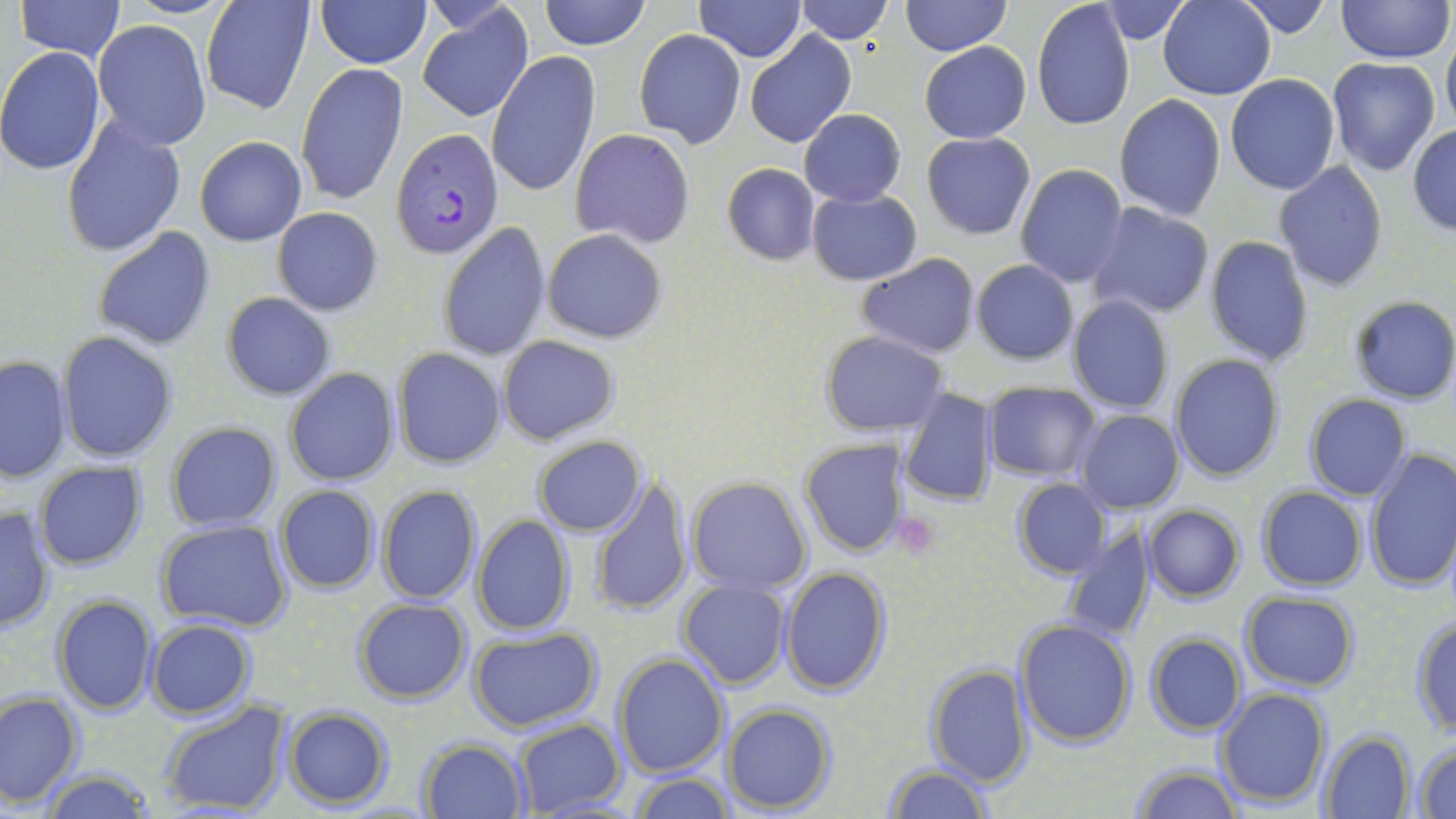 Approximate bounding boxes as named x1/y1/x2/y2 corners in pixels. Platelet locations: (x1=890, y1=513, x2=941, y2=558). Plasmodium falciparum-infected red blood cell locations: (x1=392, y1=127, x2=503, y2=259). Uninfected red blood cell locations: (x1=15, y1=0, x2=126, y2=61), (x1=117, y1=0, x2=240, y2=18), (x1=200, y1=0, x2=315, y2=115), (x1=316, y1=0, x2=430, y2=69), (x1=539, y1=0, x2=651, y2=50), (x1=695, y1=0, x2=805, y2=62), (x1=794, y1=0, x2=893, y2=44), (x1=901, y1=0, x2=1009, y2=57), (x1=1158, y1=0, x2=1275, y2=99), (x1=1233, y1=0, x2=1335, y2=39), (x1=1335, y1=0, x2=1454, y2=65), (x1=1098, y1=1, x2=1189, y2=43), (x1=1031, y1=2, x2=1136, y2=133), (x1=417, y1=4, x2=534, y2=122), (x1=92, y1=20, x2=210, y2=150), (x1=1441, y1=28, x2=1456, y2=134), (x1=634, y1=29, x2=745, y2=148), (x1=745, y1=30, x2=857, y2=149), (x1=920, y1=41, x2=1031, y2=143), (x1=0, y1=48, x2=106, y2=176), (x1=487, y1=53, x2=600, y2=198), (x1=1326, y1=57, x2=1441, y2=177), (x1=296, y1=64, x2=408, y2=205), (x1=1224, y1=74, x2=1341, y2=194), (x1=1114, y1=95, x2=1227, y2=222), (x1=799, y1=108, x2=905, y2=206), (x1=61, y1=116, x2=186, y2=258), (x1=1408, y1=124, x2=1455, y2=235), (x1=570, y1=128, x2=695, y2=248), (x1=921, y1=132, x2=1034, y2=239), (x1=195, y1=136, x2=306, y2=246), (x1=1273, y1=161, x2=1389, y2=291), (x1=722, y1=163, x2=821, y2=265), (x1=1014, y1=165, x2=1128, y2=287), (x1=806, y1=187, x2=921, y2=286), (x1=1087, y1=203, x2=1215, y2=320), (x1=273, y1=207, x2=382, y2=315), (x1=440, y1=222, x2=552, y2=361), (x1=93, y1=227, x2=216, y2=352), (x1=542, y1=229, x2=667, y2=343), (x1=1204, y1=236, x2=1315, y2=365), (x1=857, y1=253, x2=981, y2=358), (x1=971, y1=260, x2=1078, y2=365), (x1=220, y1=292, x2=337, y2=402), (x1=1066, y1=295, x2=1174, y2=413), (x1=1348, y1=295, x2=1456, y2=406), (x1=820, y1=330, x2=948, y2=437), (x1=58, y1=331, x2=178, y2=463), (x1=497, y1=336, x2=621, y2=445), (x1=391, y1=348, x2=507, y2=468), (x1=1168, y1=354, x2=1284, y2=481), (x1=1, y1=355, x2=71, y2=484), (x1=284, y1=367, x2=400, y2=487), (x1=984, y1=383, x2=1100, y2=481), (x1=897, y1=387, x2=999, y2=507), (x1=1303, y1=394, x2=1412, y2=501), (x1=1075, y1=409, x2=1182, y2=513), (x1=167, y1=421, x2=283, y2=531), (x1=533, y1=435, x2=647, y2=536), (x1=799, y1=436, x2=912, y2=558), (x1=1363, y1=448, x2=1456, y2=596), (x1=32, y1=462, x2=149, y2=571), (x1=591, y1=476, x2=694, y2=616), (x1=687, y1=476, x2=814, y2=595), (x1=1011, y1=478, x2=1111, y2=579), (x1=376, y1=484, x2=482, y2=605), (x1=275, y1=485, x2=381, y2=594), (x1=1256, y1=486, x2=1367, y2=592), (x1=1143, y1=504, x2=1244, y2=602), (x1=0, y1=507, x2=55, y2=633), (x1=472, y1=515, x2=574, y2=635), (x1=156, y1=518, x2=295, y2=635), (x1=1059, y1=526, x2=1154, y2=644), (x1=780, y1=566, x2=890, y2=697), (x1=677, y1=578, x2=791, y2=690), (x1=1241, y1=591, x2=1359, y2=690), (x1=51, y1=594, x2=157, y2=715), (x1=352, y1=598, x2=472, y2=704), (x1=1410, y1=615, x2=1456, y2=735), (x1=146, y1=618, x2=255, y2=718), (x1=1013, y1=618, x2=1137, y2=748), (x1=469, y1=627, x2=601, y2=730), (x1=1145, y1=632, x2=1246, y2=736), (x1=612, y1=652, x2=730, y2=778), (x1=923, y1=663, x2=1034, y2=788), (x1=1216, y1=688, x2=1331, y2=808), (x1=1, y1=691, x2=84, y2=806), (x1=158, y1=699, x2=291, y2=816), (x1=724, y1=704, x2=836, y2=814), (x1=283, y1=706, x2=393, y2=808), (x1=511, y1=719, x2=626, y2=819), (x1=1318, y1=730, x2=1414, y2=817), (x1=418, y1=738, x2=529, y2=818), (x1=1411, y1=741, x2=1456, y2=817), (x1=1127, y1=763, x2=1242, y2=819), (x1=881, y1=764, x2=997, y2=819), (x1=36, y1=766, x2=156, y2=819), (x1=628, y1=774, x2=736, y2=818). Slide-level diagnosis: Plasmodium falciparum. 1000x magnification. Light microscopy. May-Grünwald-Giemsa stain. Image is 1456×819 pixels. One field of a larger specimen. Thin blood smear.